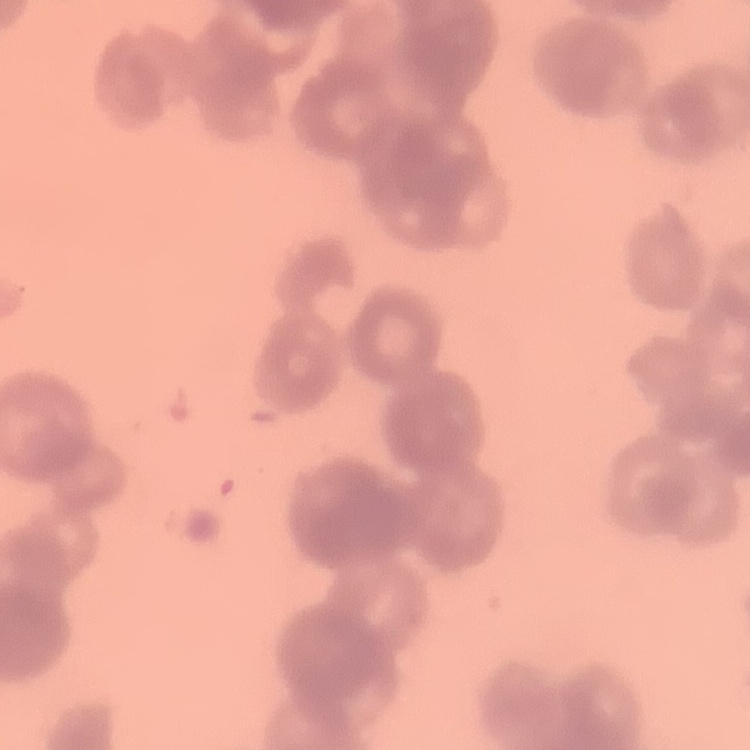 The erythrocytes exhibit rouleaux formation. Square crop of a larger photomicrograph. Stained with either Field's or Giemsa. Thin blood film.